Name the cell type shown.
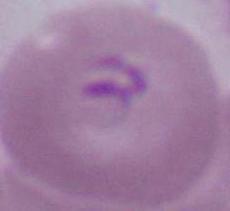
An erythrocyte.

Micrograph. 1000x magnification.